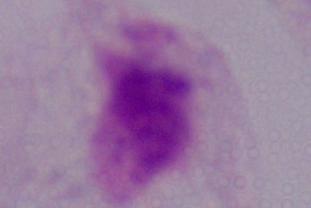
Summary:
  - Identification: trichomonad
  - Modality: photomicrograph
  - Magnification: 1000x